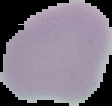

{
  "preparation": "thin blood smear",
  "image_type": "segmented cell region on a black background",
  "result": "no malaria parasites detected",
  "image_size": "112×106 pixels"
}